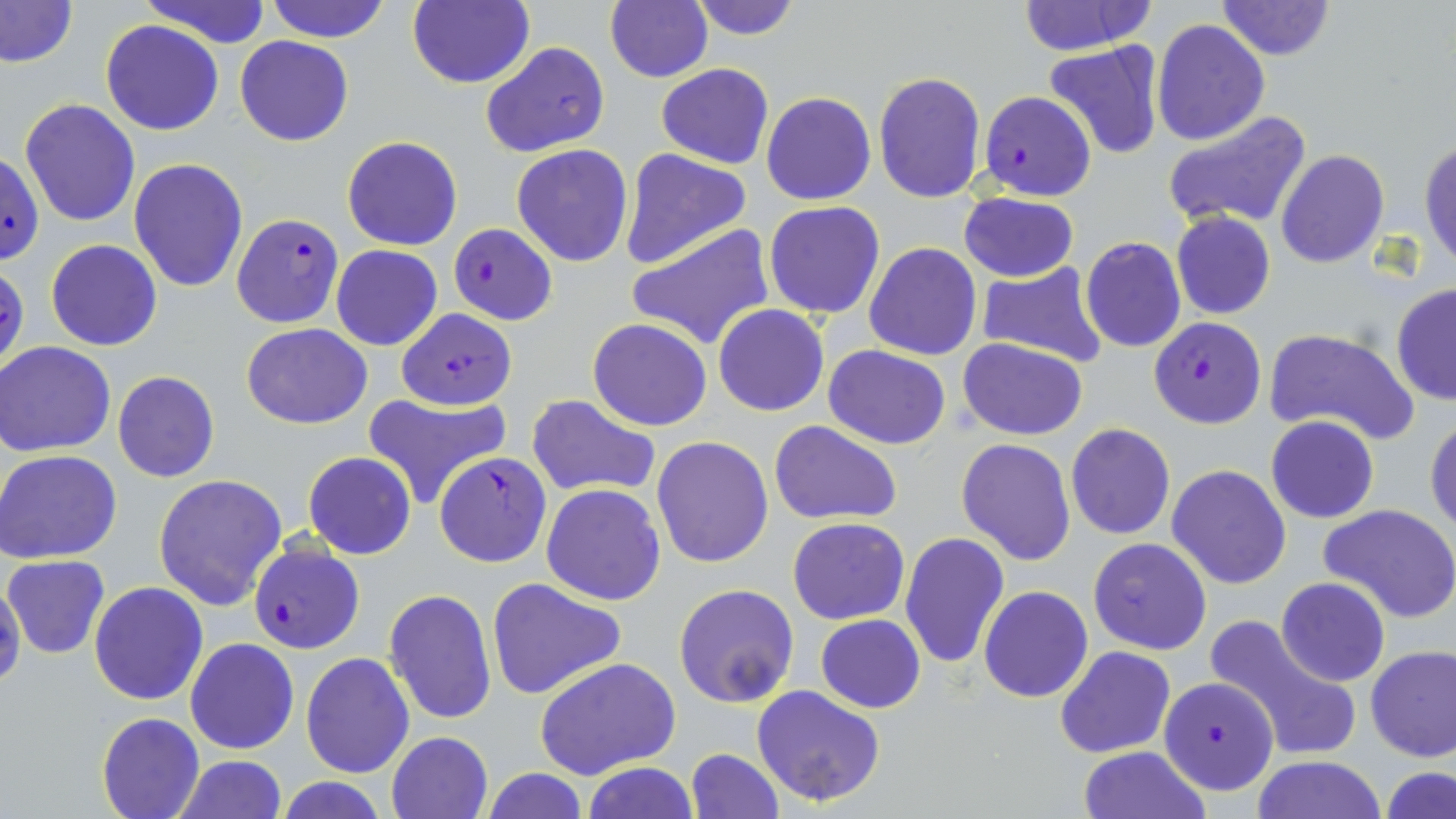
Summary:
  - Coordinate format: approximate bounding boxes as (x1, y1, x2, y2) in pixels
  - Plasmodium falciparum-infected red blood cell locations: (979, 90, 1097, 201), (2, 150, 46, 265), (231, 214, 344, 328), (447, 223, 559, 324), (0, 262, 27, 375), (398, 308, 517, 411), (1149, 316, 1267, 428), (434, 451, 552, 568), (249, 540, 365, 654), (1159, 674, 1280, 796)
  - Uninfected red blood cell locations: (0, 0, 77, 69), (140, 0, 275, 47), (264, 0, 392, 44), (407, 0, 534, 89), (605, 0, 713, 84), (688, 0, 802, 40), (1215, 0, 1336, 60), (1016, 1, 1154, 54), (1151, 19, 1270, 146), (100, 21, 224, 136), (235, 36, 353, 147), (479, 40, 610, 158), (1042, 42, 1166, 161), (656, 64, 773, 167), (872, 71, 987, 204), (760, 91, 876, 205), (19, 97, 141, 228), (1164, 109, 1312, 231), (342, 134, 463, 250), (1420, 138, 1456, 272), (512, 144, 634, 266), (619, 149, 752, 270), (1276, 149, 1389, 268), (129, 158, 249, 291), (958, 191, 1080, 283), (764, 201, 885, 319), (1170, 212, 1275, 319), (627, 222, 775, 350), (1080, 236, 1187, 353), (45, 238, 163, 351), (863, 242, 982, 361), (331, 246, 442, 351), (975, 262, 1108, 369), (1391, 283, 1456, 405), (713, 305, 828, 416), (587, 319, 713, 431), (242, 323, 372, 430), (1262, 329, 1418, 445), (957, 336, 1089, 440), (1, 341, 118, 457), (823, 344, 949, 449), (112, 370, 220, 483), (362, 392, 510, 509), (527, 395, 659, 497), (1267, 415, 1379, 522), (1426, 418, 1456, 534), (768, 420, 903, 525), (1066, 424, 1175, 540), (651, 436, 774, 568), (956, 438, 1076, 565), (0, 449, 123, 563), (303, 451, 415, 560), (1167, 464, 1293, 589), (153, 475, 290, 613), (542, 482, 667, 604), (1319, 503, 1456, 624), (787, 517, 910, 624), (899, 531, 1010, 668), (1088, 537, 1212, 655), (3, 555, 109, 658), (2, 572, 25, 690), (484, 577, 625, 700), (1277, 578, 1390, 686), (89, 582, 209, 705), (674, 583, 799, 708), (979, 584, 1093, 704), (384, 588, 498, 727), (815, 614, 925, 712), (1205, 615, 1362, 764), (186, 638, 299, 754), (1055, 645, 1176, 758), (1366, 646, 1456, 763), (301, 652, 415, 776), (534, 657, 680, 778), (752, 684, 887, 806), (97, 711, 204, 818), (386, 732, 492, 819), (1079, 746, 1206, 819), (685, 748, 783, 817), (171, 755, 289, 818), (1250, 756, 1388, 818), (580, 762, 699, 819), (1381, 766, 1455, 819), (479, 768, 589, 818), (275, 777, 387, 818)
  - Slide-level diagnosis: Plasmodium falciparum
  - Image size: 1456×819 pixels
  - Modality: light microscopy
  - Stain: May-Grünwald-Giemsa
  - Field of view: single
  - Preparation: thin blood smear
  - Magnification: 1000x